Classify this cell by malaria status.
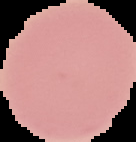

Uninfected.

Summary:
  - Preparation: thin blood smear
  - Image type: segmented cell region with the area outside set to black
  - Image size: 136×142 pixels